Locate every blood parasite and identify its species.
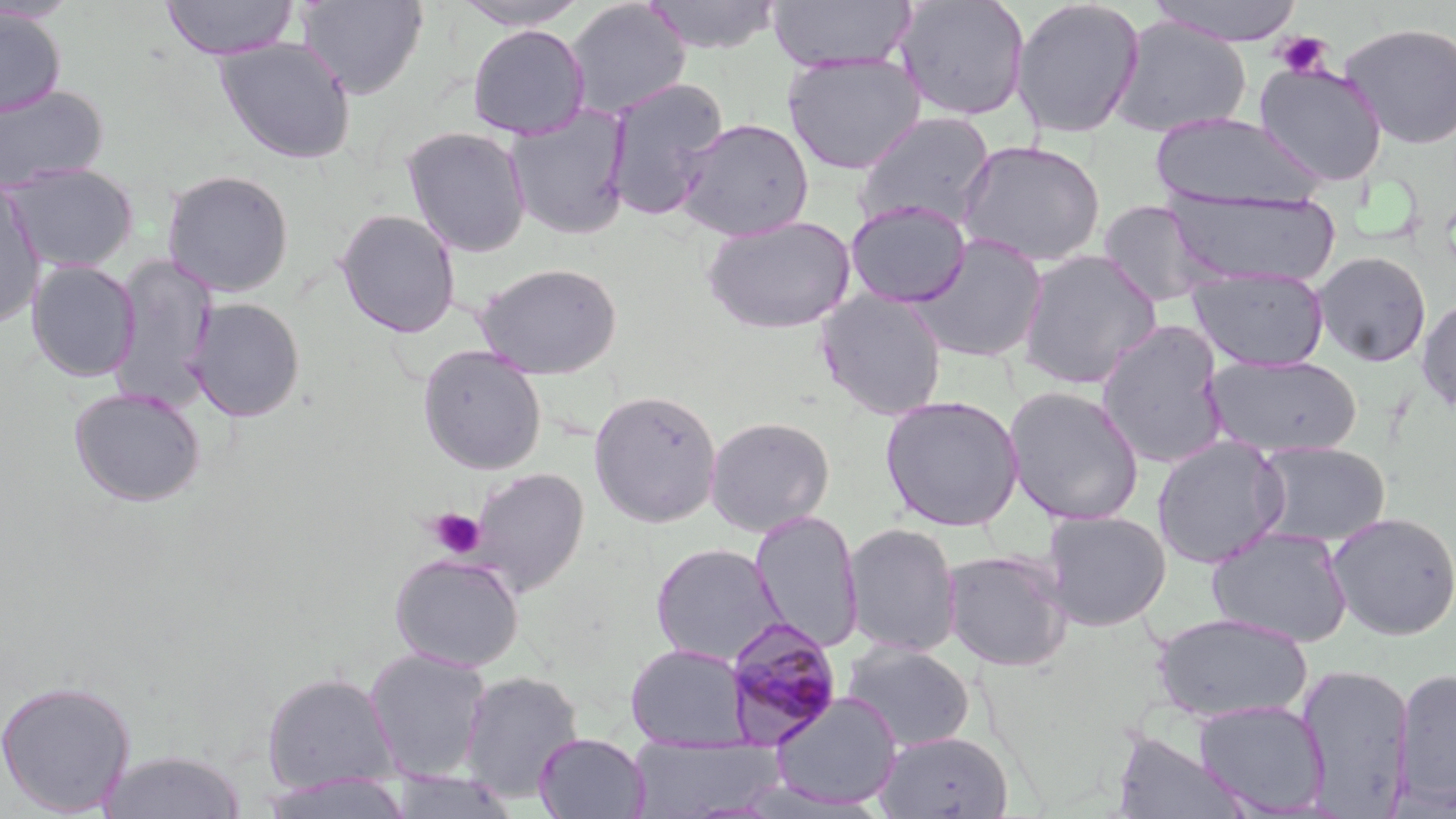
Approximate bounding boxes as [x1, y1, x2, y2] in pixels.
Plasmodium malariae-infected red blood cells: [723, 615, 845, 746].
No Plasmodium falciparum, Plasmodium ovale, Plasmodium vivax, Babesia divergens, or Trypanosoma brucei observed.

Uninfected red blood cell locations: [161, 0, 299, 60], [295, 0, 428, 100], [642, 0, 782, 54], [768, 0, 917, 73], [892, 0, 1030, 122], [1010, 0, 1145, 140], [1145, 0, 1306, 46], [451, 1, 591, 31], [565, 1, 691, 120], [0, 8, 67, 118], [1108, 15, 1250, 138], [1339, 21, 1456, 148], [466, 24, 591, 141], [214, 37, 357, 165], [782, 53, 926, 174], [1254, 61, 1389, 187], [603, 77, 729, 220], [0, 84, 109, 194], [504, 105, 631, 241], [852, 111, 996, 234], [1150, 112, 1326, 211], [676, 117, 814, 241], [401, 126, 532, 258], [957, 139, 1106, 267], [2, 162, 140, 272], [161, 168, 295, 298], [0, 179, 46, 330], [1164, 189, 1342, 288], [845, 200, 972, 308], [1097, 200, 1225, 308], [335, 208, 461, 338], [701, 214, 856, 335], [910, 233, 1049, 363], [1016, 249, 1162, 390], [1312, 251, 1432, 367], [108, 255, 218, 410], [25, 259, 141, 382], [474, 261, 623, 379], [1188, 266, 1329, 371], [816, 290, 948, 420], [189, 297, 306, 422], [1416, 298, 1456, 415], [1096, 321, 1231, 469], [418, 346, 546, 475], [1205, 353, 1364, 459], [1003, 385, 1145, 526], [69, 386, 206, 507], [588, 389, 723, 528], [880, 394, 1024, 531], [705, 416, 835, 536], [1151, 436, 1289, 569], [1252, 441, 1391, 546], [467, 467, 589, 596], [749, 509, 863, 653], [1041, 510, 1173, 631], [1326, 511, 1456, 640], [843, 522, 962, 658], [1206, 525, 1354, 647], [650, 542, 786, 667], [942, 549, 1072, 672], [388, 553, 524, 672], [1152, 612, 1313, 723], [842, 640, 976, 753], [625, 643, 750, 750], [364, 648, 491, 781], [1296, 663, 1415, 814], [1393, 666, 1456, 809], [459, 670, 584, 803], [261, 671, 399, 794], [0, 678, 137, 817], [770, 691, 903, 810], [1192, 699, 1329, 815], [875, 730, 1014, 818], [1110, 730, 1254, 819], [534, 732, 650, 819], [626, 734, 785, 817], [98, 749, 247, 819], [385, 772, 521, 818], [258, 774, 415, 818]. Platelet locations: [1272, 31, 1333, 79], [428, 509, 486, 559]. Slide-level diagnosis: Plasmodium malariae. Captured at 1000x magnification. Light microscopy. One field of a larger specimen. Image is 1456×819 pixels. May-Grünwald-Giemsa-stained preparation. Thin blood film.